State the blood parasite species.
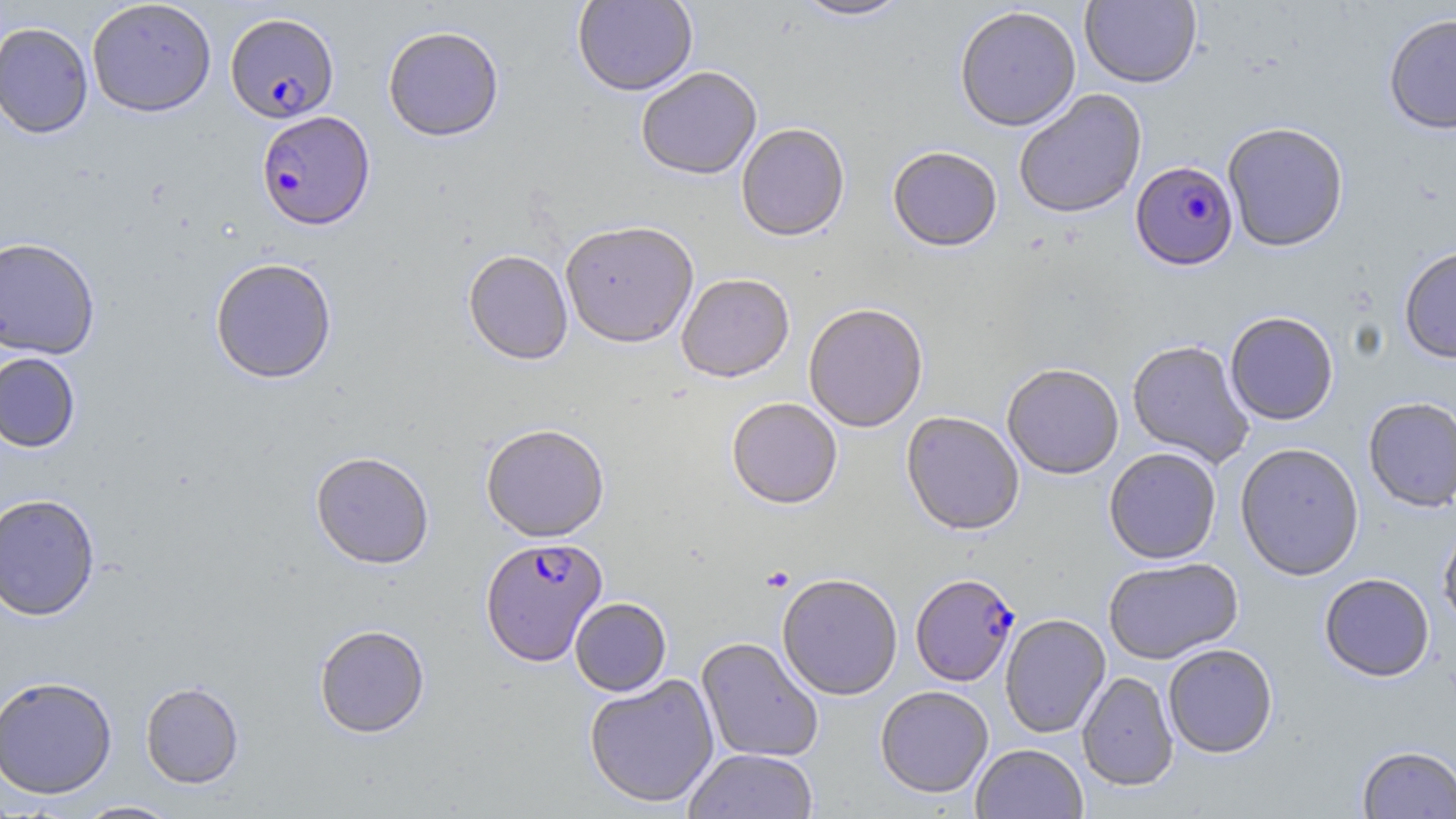
Plasmodium falciparum.

Approximate bounding boxes as named x1/y1/x2/y2 corners in pixels. Uninfected red blood cell locations: (x1=86, y1=0, x2=217, y2=117), (x1=573, y1=0, x2=698, y2=99), (x1=794, y1=0, x2=911, y2=23), (x1=1080, y1=0, x2=1201, y2=90), (x1=955, y1=8, x2=1081, y2=135), (x1=1383, y1=13, x2=1456, y2=135), (x1=0, y1=22, x2=93, y2=139), (x1=383, y1=28, x2=504, y2=144), (x1=636, y1=69, x2=762, y2=183), (x1=1014, y1=90, x2=1148, y2=221), (x1=1223, y1=124, x2=1349, y2=253), (x1=737, y1=126, x2=850, y2=245), (x1=887, y1=149, x2=1002, y2=255), (x1=560, y1=225, x2=699, y2=351), (x1=0, y1=236, x2=101, y2=359), (x1=1399, y1=247, x2=1456, y2=366), (x1=463, y1=253, x2=573, y2=368), (x1=209, y1=259, x2=338, y2=385), (x1=677, y1=276, x2=795, y2=386), (x1=804, y1=305, x2=928, y2=434), (x1=1225, y1=313, x2=1338, y2=427), (x1=1127, y1=341, x2=1254, y2=468), (x1=0, y1=352, x2=81, y2=453), (x1=1002, y1=365, x2=1124, y2=482), (x1=1363, y1=397, x2=1456, y2=513), (x1=727, y1=399, x2=842, y2=512), (x1=901, y1=413, x2=1024, y2=538), (x1=481, y1=426, x2=609, y2=544), (x1=1236, y1=444, x2=1364, y2=582), (x1=1104, y1=450, x2=1221, y2=565), (x1=310, y1=453, x2=435, y2=571), (x1=0, y1=492, x2=101, y2=622), (x1=1438, y1=518, x2=1456, y2=634), (x1=1103, y1=558, x2=1244, y2=666), (x1=1319, y1=573, x2=1435, y2=683), (x1=777, y1=576, x2=903, y2=702), (x1=570, y1=598, x2=671, y2=697), (x1=1000, y1=615, x2=1111, y2=739), (x1=314, y1=625, x2=430, y2=740), (x1=696, y1=638, x2=824, y2=763), (x1=1163, y1=645, x2=1278, y2=760), (x1=1077, y1=672, x2=1178, y2=792), (x1=584, y1=674, x2=720, y2=809), (x1=0, y1=675, x2=117, y2=799), (x1=140, y1=681, x2=245, y2=789), (x1=875, y1=687, x2=994, y2=799), (x1=971, y1=744, x2=1088, y2=819), (x1=1357, y1=745, x2=1456, y2=818), (x1=683, y1=749, x2=818, y2=819), (x1=73, y1=800, x2=183, y2=818). Platelet locations: (x1=760, y1=566, x2=793, y2=592). Plasmodium falciparum-infected red blood cell locations: (x1=225, y1=12, x2=339, y2=124), (x1=256, y1=111, x2=375, y2=232), (x1=1130, y1=162, x2=1238, y2=271), (x1=480, y1=538, x2=608, y2=668), (x1=910, y1=576, x2=1020, y2=688). Image is 1456×819 pixels. Single field of view. Thin blood film. Light microscopy. 1000x magnification. May-Grünwald-Giemsa-stained preparation.